Outline each uninfected red blood cell.
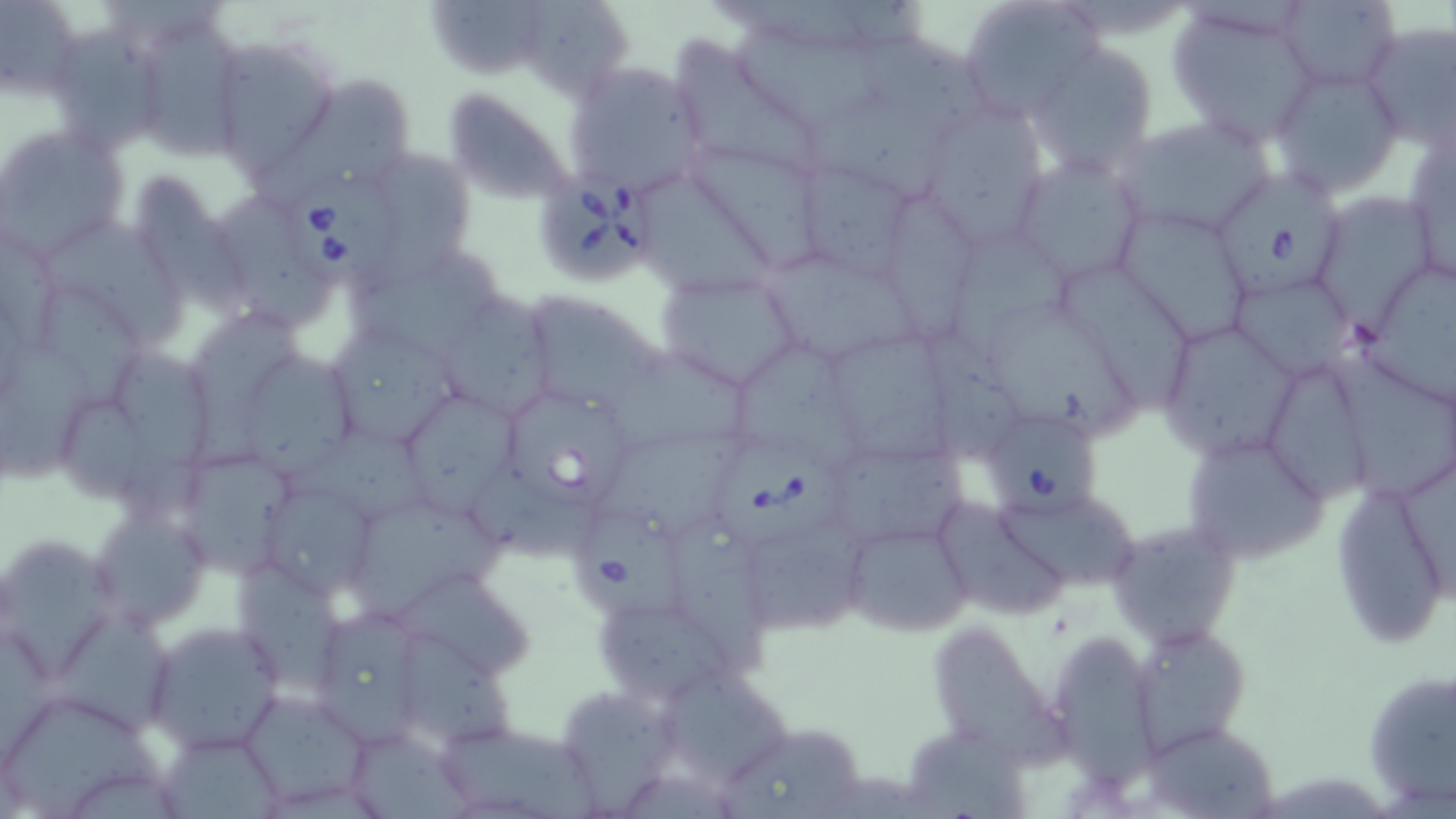

Approximate bounding boxes as (x1, y1, x2, y2) in pixels.
Uninfected red blood cells: (0, 0, 81, 99), (533, 0, 637, 105), (957, 0, 1102, 122), (1276, 0, 1401, 92), (423, 1, 546, 90), (1166, 3, 1319, 143), (127, 15, 247, 160), (1360, 21, 1456, 151), (46, 24, 168, 156), (735, 26, 895, 136), (851, 33, 998, 136), (209, 34, 343, 177), (673, 37, 823, 180), (1025, 42, 1160, 177), (562, 60, 708, 202), (1269, 64, 1403, 198), (292, 72, 412, 191), (441, 85, 580, 207), (809, 102, 968, 210), (927, 104, 1053, 256), (1112, 118, 1276, 239), (1, 125, 129, 258), (1403, 132, 1456, 288), (687, 142, 812, 272), (380, 149, 478, 287), (1010, 155, 1148, 283), (788, 157, 922, 280), (133, 172, 260, 326), (632, 179, 786, 298), (1317, 195, 1436, 342), (223, 196, 340, 332), (1118, 207, 1255, 345), (44, 217, 191, 347), (943, 236, 1081, 356), (1364, 252, 1456, 409), (352, 258, 504, 372), (765, 258, 932, 367), (655, 268, 806, 393), (1060, 269, 1198, 417), (36, 285, 153, 407), (1234, 286, 1359, 391), (517, 289, 671, 416), (437, 293, 554, 420), (984, 303, 1143, 446), (196, 307, 300, 476), (1154, 317, 1302, 462), (322, 324, 464, 454), (0, 332, 97, 490), (923, 332, 1022, 466), (826, 338, 959, 472), (604, 350, 767, 457), (113, 354, 226, 522), (730, 354, 867, 477), (1336, 356, 1456, 497), (243, 357, 370, 480), (1272, 363, 1373, 513), (58, 387, 152, 501), (408, 395, 527, 522), (283, 430, 452, 534), (1181, 433, 1332, 562), (599, 443, 756, 537), (831, 450, 973, 548), (179, 454, 293, 578), (476, 461, 605, 567), (1330, 478, 1450, 649), (256, 488, 379, 604), (997, 500, 1145, 590), (936, 502, 1066, 617), (87, 506, 215, 631), (355, 506, 507, 619), (673, 515, 772, 679), (841, 516, 974, 639), (1108, 521, 1243, 646), (740, 528, 871, 637), (0, 540, 134, 683), (234, 565, 352, 698), (393, 579, 535, 680), (310, 603, 434, 750), (588, 612, 739, 701), (51, 619, 178, 730), (142, 621, 285, 753), (1130, 622, 1249, 754), (936, 629, 1070, 772), (1046, 632, 1160, 787), (402, 637, 524, 744), (653, 657, 793, 789), (1362, 665, 1455, 815), (556, 684, 678, 812), (236, 688, 373, 810), (6, 699, 168, 819), (430, 717, 602, 819), (716, 721, 871, 819), (1141, 722, 1281, 816), (913, 729, 1032, 819), (159, 736, 288, 819), (356, 740, 483, 819).

Babesia divergens-infected red blood cell locations: (539, 166, 654, 286), (286, 170, 404, 290), (1215, 170, 1341, 305), (506, 396, 631, 514), (984, 417, 1098, 522), (708, 445, 850, 550), (577, 514, 688, 625). Slide-level diagnosis: Babesia divergens. May-Grünwald-Giemsa stain. Optical microscopy. One field of a larger specimen. Thin blood film. Image is 1456×819 pixels. 1000x magnification.